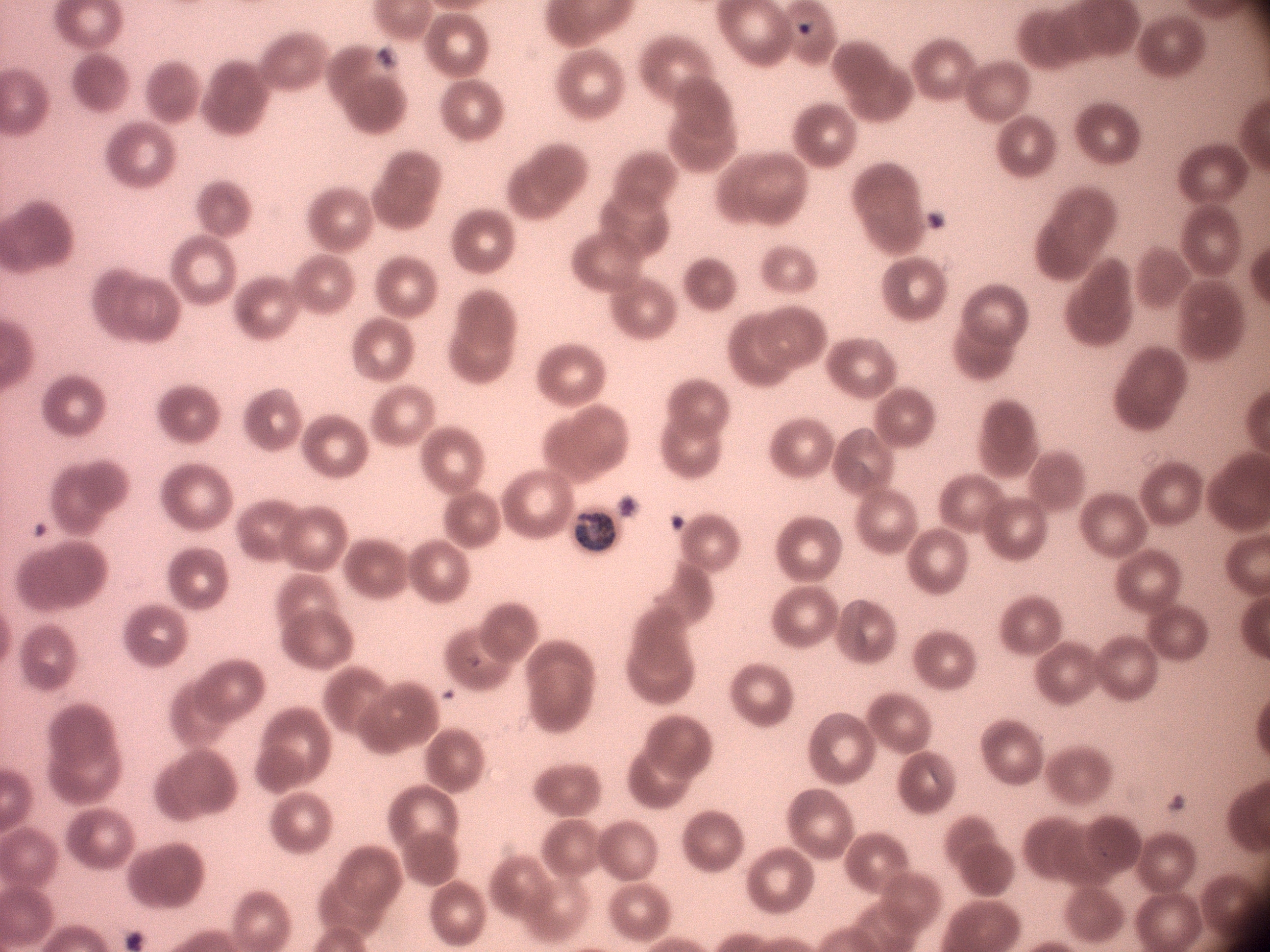
Approximate bounding boxes as (x1, y1, x2, y2) in pixels, from the source annotation, which is not necessarily exhaustive. Trophozoite locations: (575, 509, 615, 553). Giemsa stain. Captured at 100x magnification. Species: Plasmodium malariae. Image is 1270×952 pixels. Single field of view. Thin blood smear. Leica DM2000 optical microscope with a built-in camera.